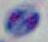
Micrograph. Toxoplasma gondii is shown. 1000x magnification.